Point out each leukocyte.
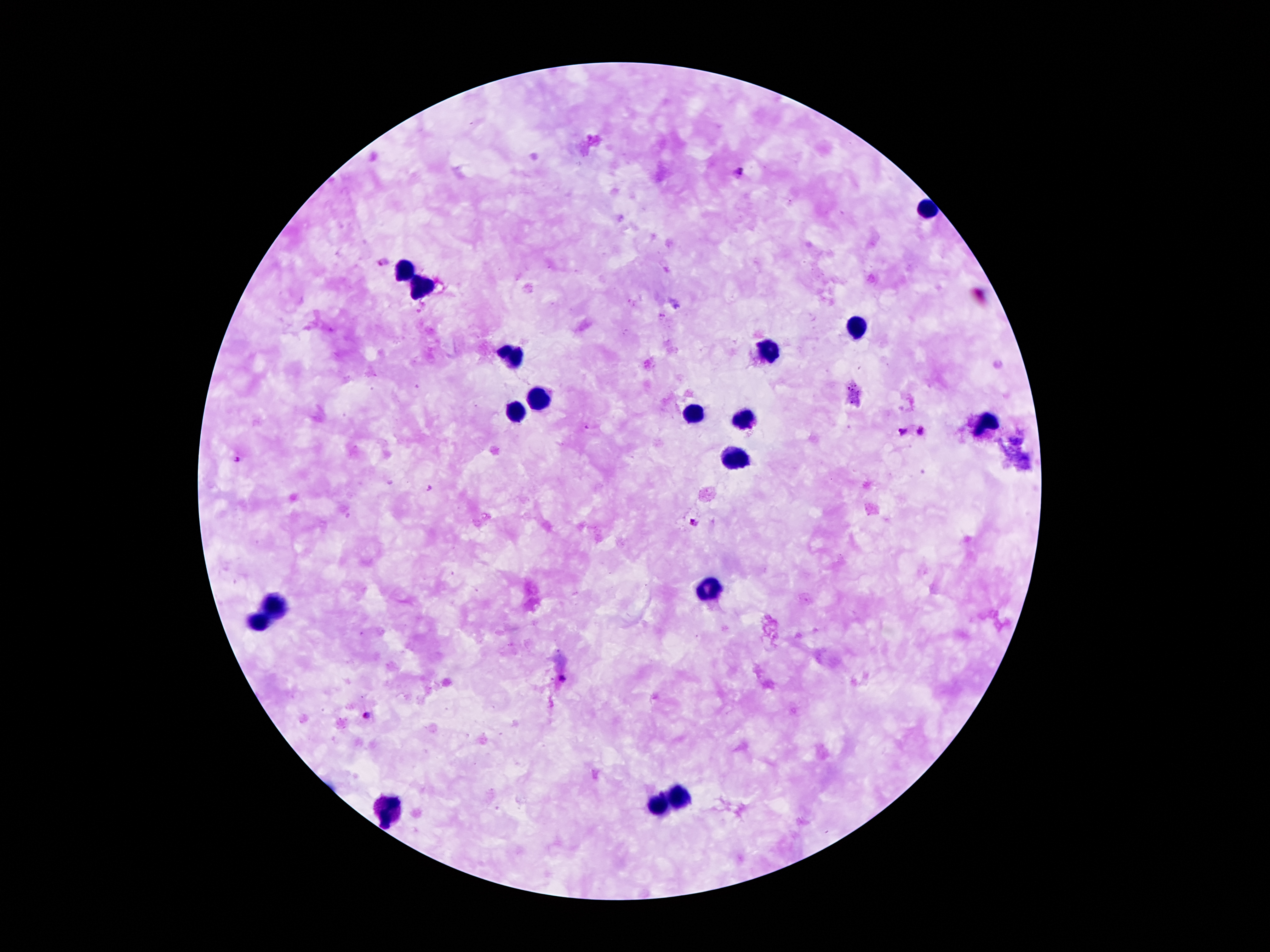

Approximate object centers, in pixels from the top-left corner.
Leukocytes: (x=926, y=210), (x=405, y=271), (x=419, y=284), (x=859, y=329), (x=770, y=348), (x=511, y=356), (x=538, y=398), (x=516, y=410), (x=696, y=414), (x=743, y=414), (x=983, y=422), (x=736, y=459), (x=706, y=588), (x=274, y=604), (x=256, y=620), (x=679, y=800), (x=657, y=805), (x=387, y=812).

Malaria parasite locations: (x=737, y=172), (x=381, y=261), (x=903, y=431), (x=922, y=433), (x=238, y=463), (x=694, y=522), (x=561, y=680), (x=367, y=716). Smartphone photograph taken through the microscope eyepiece. Patient malaria status: infected with Plasmodium falciparum. Thick blood film. Single field of view. Image is 1270×952 pixels. Giemsa stain. 100x magnification.